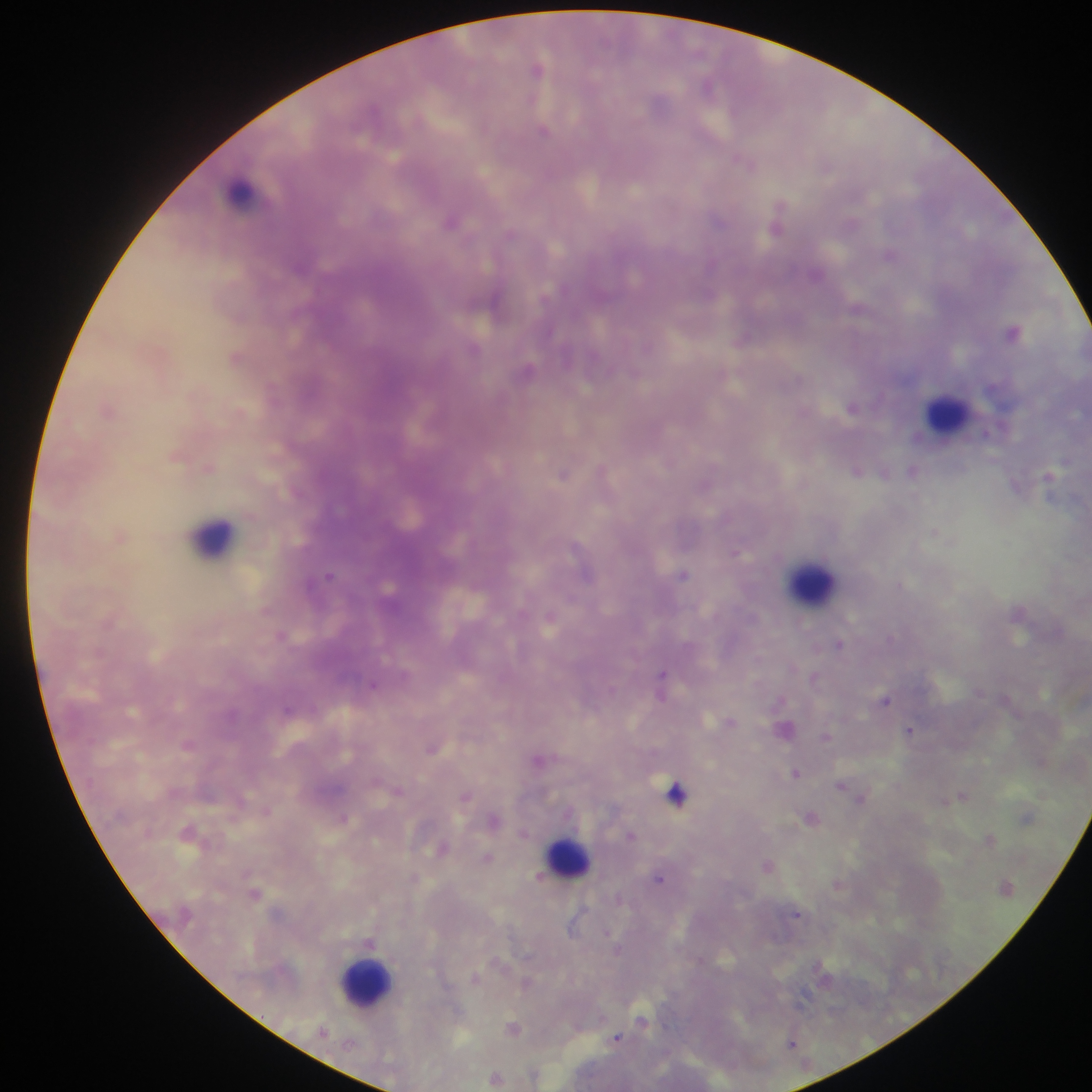

Approximate centers as [x, y] in pixels.
Summary:
  - Plasmodium parasite locations: [537, 68], [708, 86], [543, 130], [743, 160], [778, 217], [451, 220], [510, 233], [890, 255], [1013, 331], [853, 406], [209, 468], [856, 470], [912, 471], [564, 473], [934, 533], [737, 552], [684, 574], [329, 575], [899, 584], [281, 634], [840, 644], [661, 675], [374, 685], [886, 700], [288, 709], [731, 722], [909, 730], [826, 736], [188, 745], [433, 748], [538, 760], [795, 772], [841, 785], [398, 790], [677, 793], [963, 795], [466, 796], [861, 798], [266, 811], [344, 817], [631, 835], [990, 838], [441, 849], [488, 858], [767, 865], [540, 877], [660, 878], [255, 893], [797, 914], [370, 942], [475, 977], [803, 996], [643, 1020], [513, 1028], [617, 1038], [791, 1043], [495, 1078]
  - Leukocyte locations: [245, 193], [947, 413], [213, 536], [812, 579], [568, 855], [366, 978]
  - Field of view: single
  - Image size: 1092×1092 pixels
  - Country: Ghana
  - Preparation: thick blood smear
  - Capture: mobile-phone photograph through a microscope